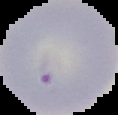

Summary:
  - Malaria status: uninfected
  - Preparation: thin blood smear
  - Image size: 118×115 pixels
  - Image type: segmented cell region with the area outside set to black